Report the malaria status of this cell.
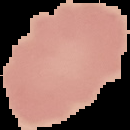

It is uninfected.

Image is 130×130 pixels. From a thin blood smear. Cell region segmented out of the field of view; the surrounding area is masked to black.